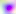
identification: Toxoplasma gondii
magnification: 400x
modality: micrograph